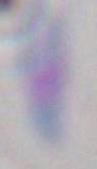

Summary:
  - Identification: Toxoplasma gondii
  - Magnification: 1000x
  - Modality: photomicrograph